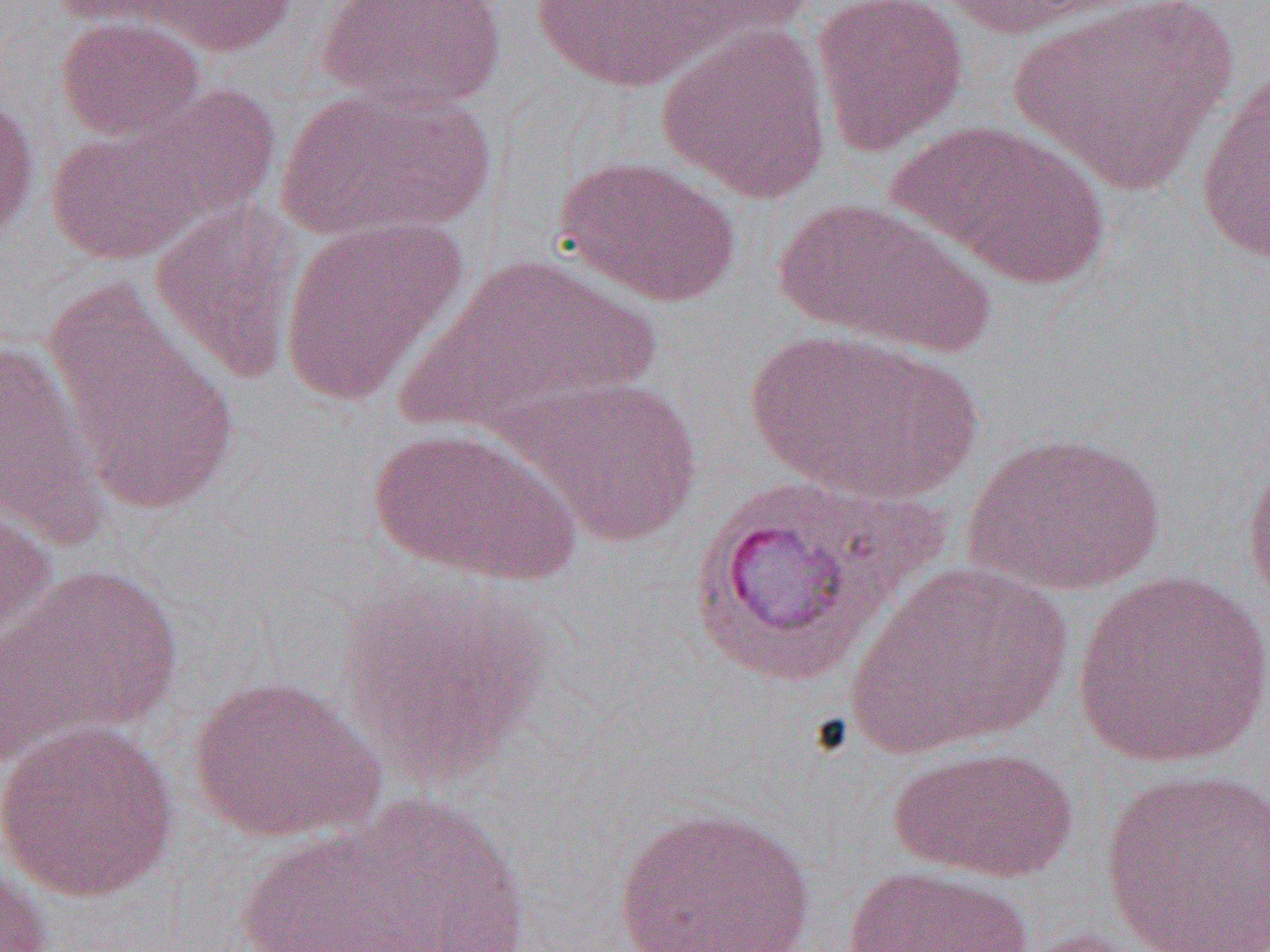
slide_level_diagnosis: Plasmodium vivax
modality: light microscopy
field_of_view: one of a larger specimen
image_size: 1270×952 pixels
preparation: thin blood film
uninfected_red_blood_cell_locations: 'approximate bounding boxes as [x1, y1, x2, y2] in pixels: [47, 0, 198, 28], [127, 0, 299, 57], [315, 0, 507, 113], [652, 0, 823, 49], [812, 0, 969, 155], [932, 0, 1134, 40], [1008, 0, 1237, 192], [526, 1, 730, 92], [55, 16, 207, 143], [656, 22, 832, 203], [1194, 71, 1270, 265], [275, 84, 496, 241], [68, 86, 285, 248], [0, 93, 40, 245], [890, 119, 1110, 290], [45, 123, 210, 266], [556, 155, 742, 307], [770, 197, 994, 358], [150, 200, 304, 382], [277, 215, 467, 407], [400, 254, 665, 433], [45, 284, 240, 517], [745, 329, 980, 504], [0, 338, 109, 547], [500, 376, 704, 546], [368, 426, 579, 583], [964, 430, 1165, 598], [1242, 441, 1270, 611], [686, 477, 930, 685], [0, 487, 57, 645], [1, 562, 183, 761], [849, 562, 1072, 756], [1070, 569, 1269, 771], [338, 579, 546, 786], [187, 674, 385, 844], [1, 718, 179, 903], [888, 745, 1078, 884], [1100, 768, 1270, 951], [305, 793, 533, 952], [611, 806, 818, 952], [227, 819, 460, 952], [0, 863, 52, 952], [841, 865, 1034, 952], [1018, 928, 1165, 952]'
magnification: 1000x